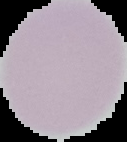

Result: no Plasmodium parasites detected. From a thin blood film. Segmented cell region on a black background. Image is 127×142 pixels.